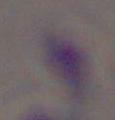
Summary:
  - Modality: micrograph
  - Identification: Toxoplasma gondii
  - Magnification: 1000x